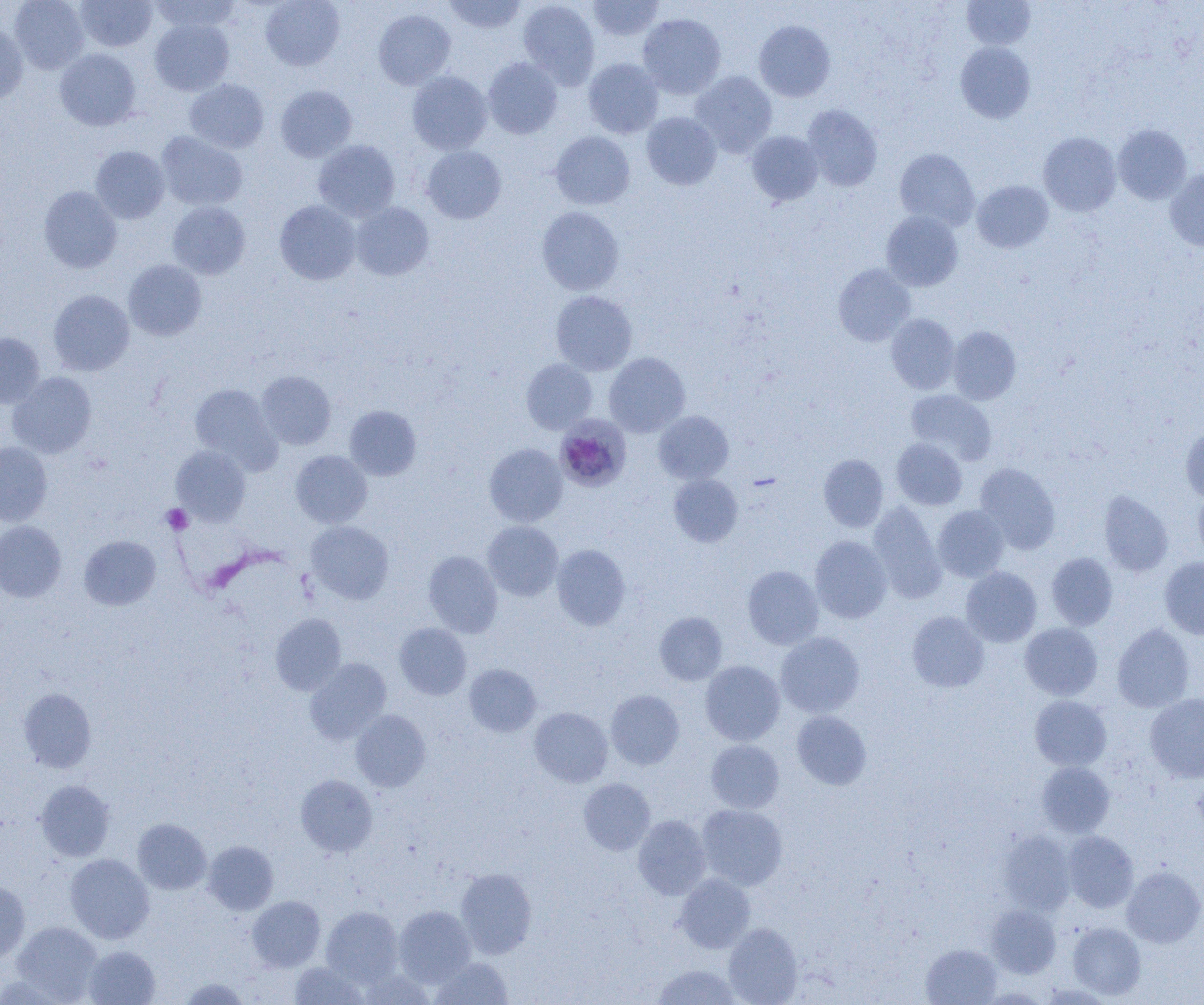
Plasmodium malariae-infected red blood cell locations = approximate bounding boxes as named x1/y1/x2/y2 corners in pixels: (x1=556, y1=410, x2=629, y2=492)
slide-level diagnosis = Plasmodium malariae
field of view = single
platelet locations = approximate bounding boxes as named x1/y1/x2/y2 corners in pixels: (x1=161, y1=505, x2=193, y2=534)
modality = optical microscopy
preparation = thin blood film
uninfected red blood cell locations = approximate bounding boxes as named x1/y1/x2/y2 corners in pixels: (x1=9, y1=0, x2=90, y2=74), (x1=148, y1=0, x2=241, y2=33), (x1=261, y1=0, x2=345, y2=71), (x1=443, y1=0, x2=527, y2=33), (x1=517, y1=0, x2=600, y2=89), (x1=588, y1=0, x2=663, y2=41), (x1=961, y1=0, x2=1035, y2=50), (x1=75, y1=1, x2=157, y2=52), (x1=373, y1=9, x2=456, y2=89), (x1=638, y1=13, x2=726, y2=98), (x1=150, y1=18, x2=234, y2=95), (x1=753, y1=20, x2=835, y2=102), (x1=0, y1=22, x2=29, y2=104), (x1=955, y1=42, x2=1035, y2=123), (x1=55, y1=48, x2=142, y2=130), (x1=482, y1=57, x2=563, y2=139), (x1=583, y1=58, x2=664, y2=138), (x1=690, y1=70, x2=777, y2=157), (x1=407, y1=71, x2=492, y2=155), (x1=184, y1=78, x2=270, y2=154), (x1=275, y1=84, x2=357, y2=162), (x1=802, y1=105, x2=883, y2=191), (x1=642, y1=112, x2=721, y2=189), (x1=1113, y1=124, x2=1192, y2=204), (x1=746, y1=130, x2=824, y2=206), (x1=156, y1=131, x2=248, y2=211), (x1=550, y1=131, x2=635, y2=209), (x1=1038, y1=132, x2=1120, y2=216), (x1=313, y1=139, x2=400, y2=222), (x1=90, y1=146, x2=169, y2=223), (x1=422, y1=146, x2=506, y2=224), (x1=894, y1=148, x2=979, y2=230), (x1=1165, y1=167, x2=1204, y2=251), (x1=972, y1=180, x2=1054, y2=253), (x1=39, y1=186, x2=122, y2=273), (x1=274, y1=200, x2=361, y2=284), (x1=168, y1=201, x2=250, y2=279), (x1=351, y1=202, x2=434, y2=281), (x1=536, y1=206, x2=624, y2=295), (x1=881, y1=211, x2=963, y2=291), (x1=123, y1=260, x2=207, y2=341), (x1=833, y1=263, x2=916, y2=346), (x1=48, y1=289, x2=134, y2=375), (x1=550, y1=290, x2=638, y2=375), (x1=886, y1=314, x2=960, y2=394), (x1=947, y1=326, x2=1021, y2=404), (x1=0, y1=332, x2=44, y2=408), (x1=604, y1=352, x2=690, y2=437), (x1=521, y1=359, x2=597, y2=434), (x1=7, y1=371, x2=97, y2=458), (x1=256, y1=371, x2=336, y2=449), (x1=190, y1=383, x2=281, y2=472), (x1=905, y1=390, x2=996, y2=465), (x1=345, y1=405, x2=422, y2=480), (x1=653, y1=410, x2=733, y2=484), (x1=1180, y1=424, x2=1204, y2=503), (x1=891, y1=438, x2=967, y2=510), (x1=0, y1=441, x2=52, y2=525), (x1=484, y1=443, x2=567, y2=527), (x1=171, y1=444, x2=251, y2=525), (x1=290, y1=450, x2=372, y2=528), (x1=818, y1=454, x2=888, y2=532), (x1=975, y1=462, x2=1061, y2=554), (x1=668, y1=473, x2=742, y2=547), (x1=1193, y1=489, x2=1204, y2=562), (x1=1099, y1=490, x2=1173, y2=577), (x1=867, y1=501, x2=946, y2=603), (x1=933, y1=505, x2=1009, y2=582), (x1=0, y1=521, x2=66, y2=602), (x1=306, y1=521, x2=394, y2=604), (x1=482, y1=521, x2=563, y2=601), (x1=79, y1=535, x2=161, y2=610), (x1=810, y1=535, x2=892, y2=623), (x1=551, y1=544, x2=631, y2=631), (x1=423, y1=550, x2=502, y2=637), (x1=1046, y1=552, x2=1118, y2=630), (x1=1160, y1=556, x2=1204, y2=639), (x1=742, y1=565, x2=823, y2=649), (x1=961, y1=567, x2=1042, y2=647), (x1=907, y1=611, x2=989, y2=692), (x1=655, y1=612, x2=727, y2=685), (x1=270, y1=613, x2=346, y2=695), (x1=394, y1=622, x2=471, y2=699), (x1=1020, y1=623, x2=1102, y2=700), (x1=1112, y1=623, x2=1195, y2=712), (x1=775, y1=632, x2=864, y2=717), (x1=305, y1=658, x2=391, y2=743), (x1=700, y1=660, x2=785, y2=745), (x1=464, y1=664, x2=541, y2=737), (x1=18, y1=688, x2=96, y2=773), (x1=605, y1=689, x2=684, y2=769), (x1=1145, y1=693, x2=1204, y2=783), (x1=1030, y1=696, x2=1112, y2=771), (x1=529, y1=707, x2=613, y2=787), (x1=351, y1=710, x2=431, y2=791), (x1=792, y1=711, x2=872, y2=789), (x1=706, y1=740, x2=784, y2=813), (x1=1037, y1=762, x2=1115, y2=837), (x1=295, y1=774, x2=377, y2=856), (x1=579, y1=777, x2=655, y2=855), (x1=36, y1=780, x2=115, y2=861), (x1=696, y1=804, x2=787, y2=890), (x1=633, y1=815, x2=710, y2=899), (x1=133, y1=818, x2=211, y2=894), (x1=999, y1=830, x2=1075, y2=915), (x1=1062, y1=831, x2=1138, y2=912), (x1=203, y1=840, x2=278, y2=914), (x1=65, y1=854, x2=154, y2=943), (x1=1122, y1=866, x2=1204, y2=947), (x1=456, y1=868, x2=537, y2=958), (x1=675, y1=873, x2=755, y2=953), (x1=0, y1=881, x2=30, y2=963), (x1=247, y1=896, x2=325, y2=971), (x1=986, y1=904, x2=1061, y2=977), (x1=394, y1=905, x2=476, y2=987), (x1=321, y1=906, x2=403, y2=986), (x1=11, y1=921, x2=103, y2=1002), (x1=1067, y1=922, x2=1146, y2=999), (x1=723, y1=923, x2=803, y2=1005), (x1=922, y1=944, x2=1001, y2=1004), (x1=83, y1=945, x2=160, y2=1004), (x1=430, y1=957, x2=514, y2=1004), (x1=290, y1=962, x2=368, y2=1004), (x1=652, y1=963, x2=743, y2=1004), (x1=360, y1=969, x2=434, y2=1005), (x1=178, y1=977, x2=251, y2=1004)
magnification = 1000x
image size = 1204×1005 pixels